Identify the preparation type.
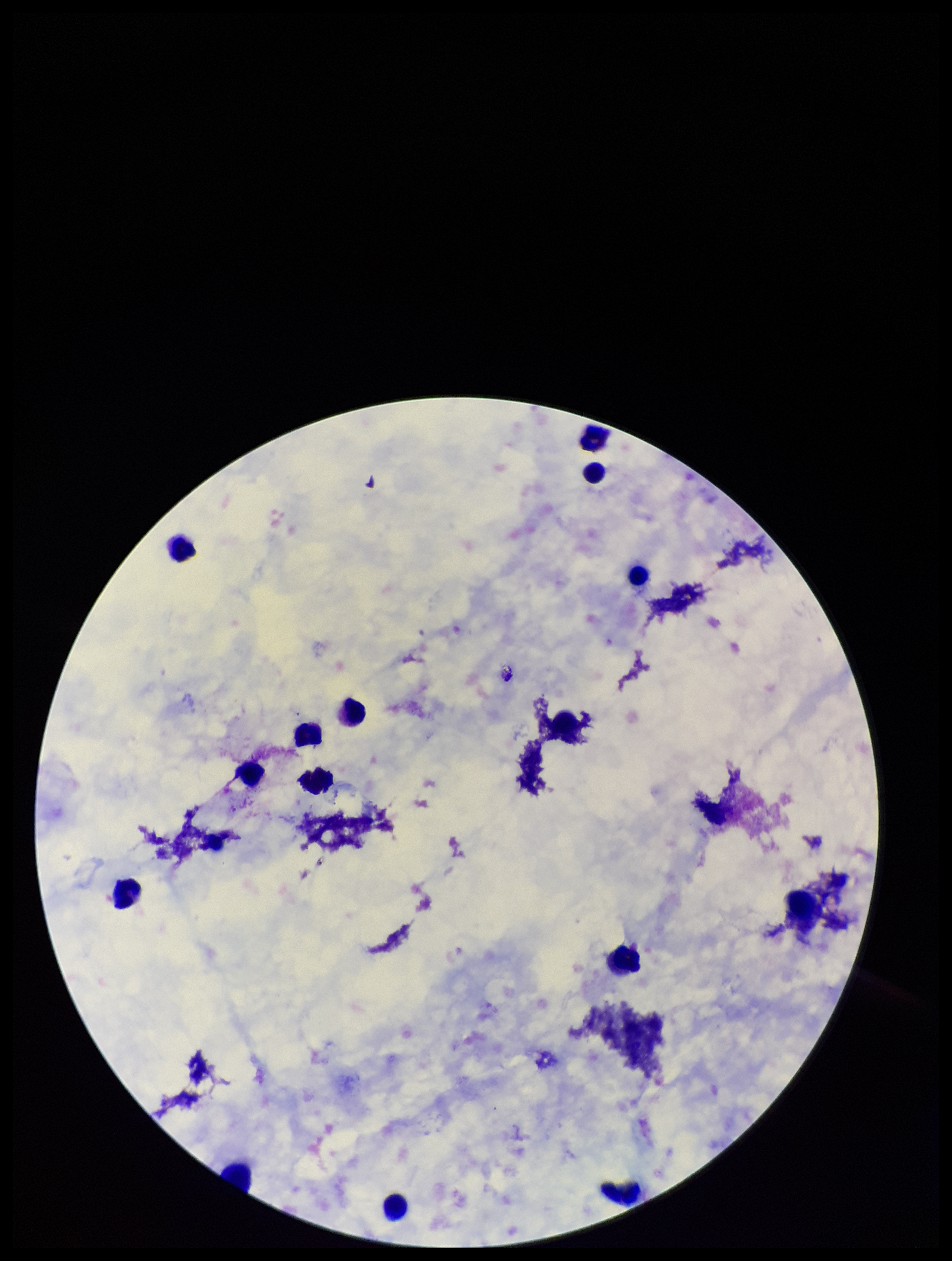

It is a thick blood smear.

Summary:
  - Field of view: one from this slide
  - Leukocyte count: 14
  - Plasmodium parasites: none identified
  - Image size: 952×1261 pixels
  - Parasite count: 0
  - Patient malaria status: negative
  - Capture: smartphone photograph through the microscope eyepiece
  - Stain: Giemsa